Assess the morphology of the red blood cells.
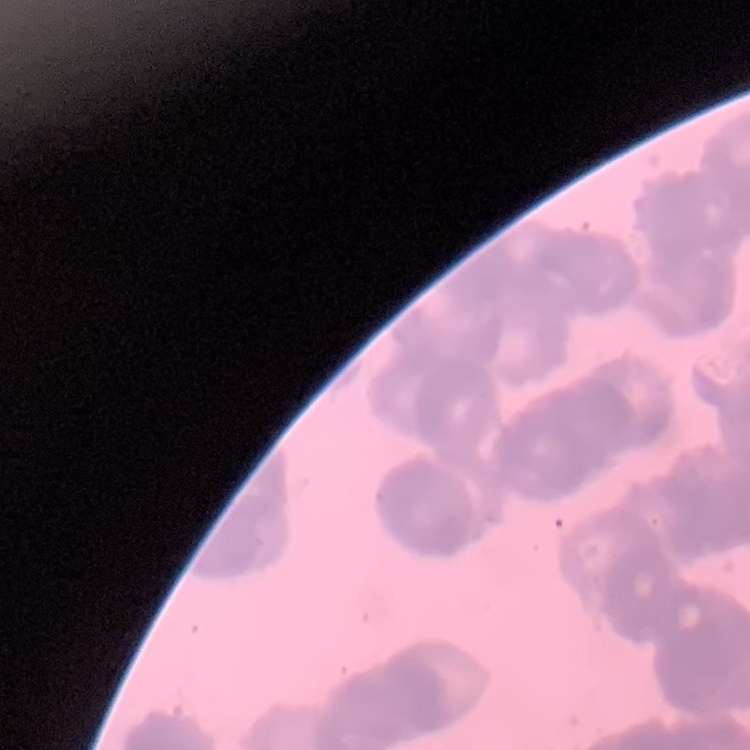
They show rouleaux formation.

stain = Field's or Giemsa
preparation = thin blood film
image type = square crop of a larger photomicrograph